Locate platelets.
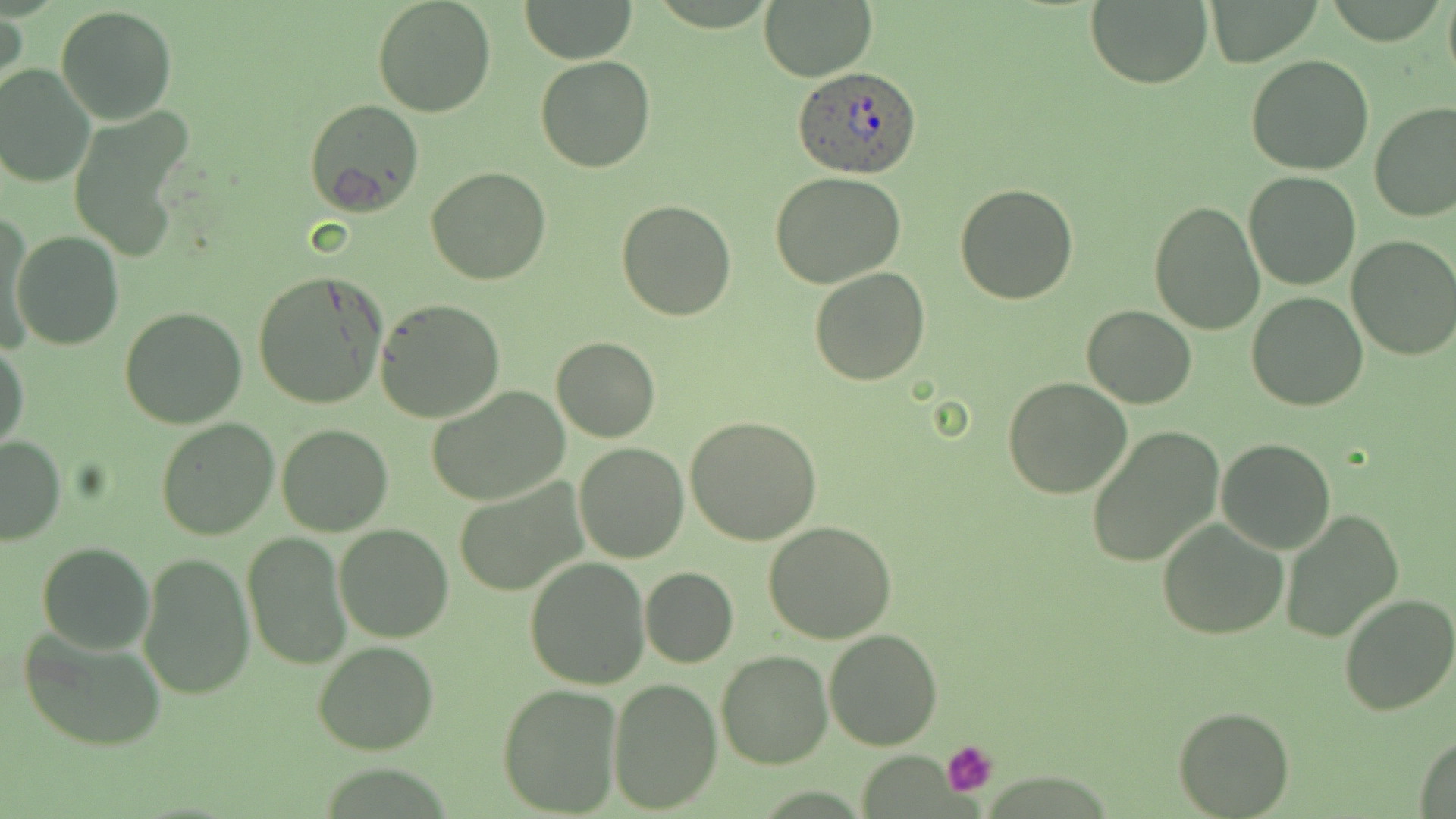
Approximate bounding boxes as named x1/y1/x2/y2 corners in pixels.
Platelets: (x1=943, y1=740, x2=999, y2=796).

Summary:
  - Plasmodium ovale-infected red blood cell locations: (x1=792, y1=66, x2=922, y2=179)
  - Uninfected red blood cell locations: (x1=371, y1=0, x2=496, y2=118), (x1=758, y1=0, x2=877, y2=82), (x1=1444, y1=0, x2=1456, y2=89), (x1=518, y1=1, x2=638, y2=64), (x1=1085, y1=1, x2=1212, y2=89), (x1=1205, y1=1, x2=1319, y2=66), (x1=55, y1=6, x2=177, y2=125), (x1=1, y1=8, x2=26, y2=107), (x1=535, y1=54, x2=656, y2=174), (x1=1244, y1=55, x2=1374, y2=174), (x1=0, y1=65, x2=95, y2=188), (x1=303, y1=99, x2=425, y2=215), (x1=1369, y1=102, x2=1456, y2=223), (x1=68, y1=111, x2=195, y2=261), (x1=425, y1=167, x2=550, y2=285), (x1=768, y1=171, x2=909, y2=291), (x1=1244, y1=172, x2=1362, y2=292), (x1=952, y1=182, x2=1078, y2=304), (x1=615, y1=198, x2=740, y2=321), (x1=1149, y1=201, x2=1265, y2=336), (x1=2, y1=214, x2=35, y2=350), (x1=10, y1=229, x2=124, y2=351), (x1=1346, y1=237, x2=1456, y2=360), (x1=809, y1=266, x2=929, y2=385), (x1=252, y1=270, x2=389, y2=409), (x1=1246, y1=290, x2=1369, y2=411), (x1=375, y1=299, x2=506, y2=424), (x1=1082, y1=306, x2=1197, y2=408), (x1=118, y1=307, x2=248, y2=429), (x1=551, y1=335, x2=660, y2=443), (x1=1, y1=341, x2=28, y2=453), (x1=1002, y1=377, x2=1130, y2=498), (x1=425, y1=386, x2=570, y2=506), (x1=685, y1=414, x2=821, y2=546), (x1=153, y1=417, x2=279, y2=540), (x1=276, y1=424, x2=393, y2=536), (x1=1085, y1=425, x2=1225, y2=568), (x1=0, y1=434, x2=65, y2=546), (x1=1217, y1=438, x2=1335, y2=554), (x1=573, y1=442, x2=688, y2=563), (x1=454, y1=477, x2=588, y2=596), (x1=1279, y1=508, x2=1404, y2=643), (x1=1156, y1=519, x2=1291, y2=639), (x1=334, y1=523, x2=454, y2=642), (x1=763, y1=523, x2=897, y2=643), (x1=242, y1=532, x2=351, y2=670), (x1=38, y1=542, x2=154, y2=654), (x1=138, y1=551, x2=255, y2=700), (x1=524, y1=556, x2=652, y2=688), (x1=639, y1=565, x2=738, y2=668), (x1=1336, y1=593, x2=1456, y2=715), (x1=19, y1=626, x2=170, y2=752), (x1=825, y1=630, x2=941, y2=750), (x1=312, y1=639, x2=440, y2=754), (x1=715, y1=650, x2=832, y2=770), (x1=608, y1=679, x2=721, y2=811), (x1=497, y1=684, x2=623, y2=815), (x1=1173, y1=706, x2=1294, y2=817), (x1=1411, y1=732, x2=1456, y2=817)
  - Slide-level diagnosis: Plasmodium ovale
  - Modality: light microscopy
  - Image size: 1456×819 pixels
  - Preparation: thin blood film
  - Magnification: 1000x
  - Field of view: one of a larger specimen
  - Stain: May-Grünwald-Giemsa